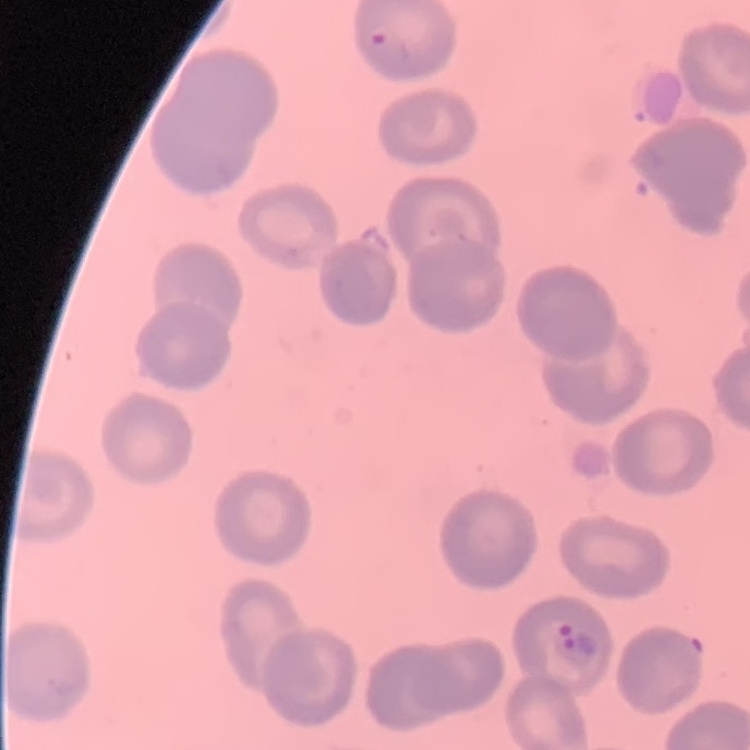

Summary:
  - Erythrocyte morphology: no rouleaux formation
  - Preparation: thin peripheral smear
  - Stain: Field's or Giemsa
  - Image type: one tile cut from a larger photomicrograph